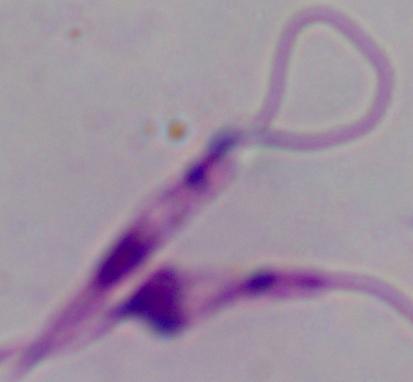 Photomicrograph. A Leishmania parasite is seen. 1000x magnification.